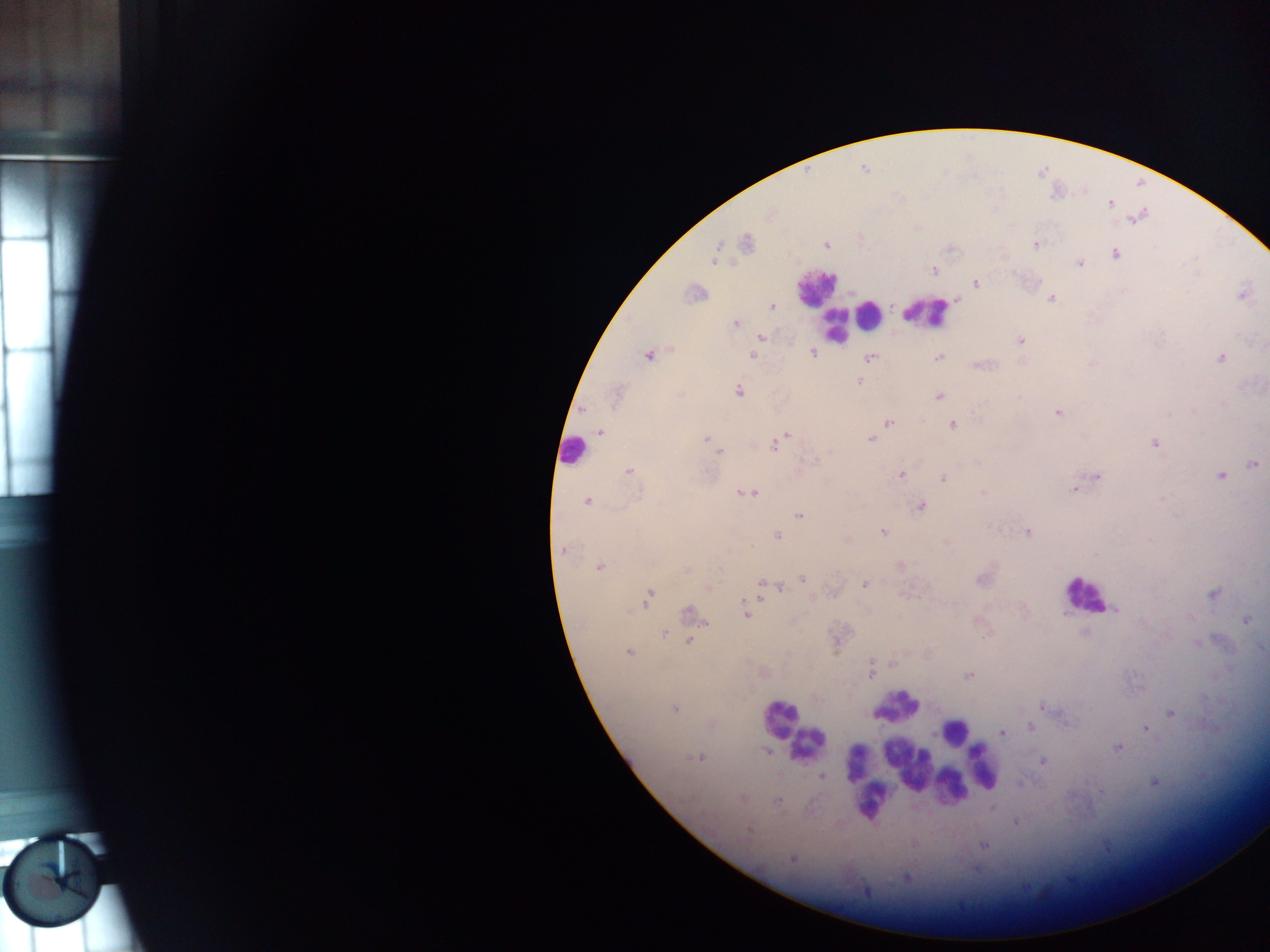
malaria parasite locations = approximate centers as {x, y} in pixels: {863, 167}, {1110, 204}, {746, 242}, {826, 244}, {1035, 244}, {1115, 254}, {716, 255}, {1080, 263}, {933, 269}, {975, 282}, {695, 293}, {1242, 294}, {1050, 298}, {772, 306}, {734, 323}, {760, 337}, {1020, 340}, {813, 352}, {648, 354}, {752, 354}, {938, 357}, {1219, 357}, {870, 358}, {859, 381}, {738, 391}, {616, 395}, {939, 396}, {1058, 412}, {888, 422}, {952, 424}, {599, 432}, {788, 434}, {707, 438}, {869, 439}, {776, 442}, {1154, 442}, {713, 448}, {719, 451}, {1252, 463}, {628, 471}, {901, 474}, {1221, 475}, {1096, 476}, {943, 478}, {1082, 484}, {1075, 488}, {747, 493}, {587, 501}, {920, 506}, {799, 515}, {883, 532}, {1028, 533}, {777, 535}, {563, 550}, {598, 566}, {899, 566}, {686, 569}, {981, 577}, {803, 580}, {864, 584}, {761, 585}, {780, 587}, {708, 588}, {1214, 593}, {647, 598}, {1022, 607}, {1116, 609}, {689, 614}, {747, 614}, {1246, 619}, {1085, 632}, {663, 634}, {691, 637}, {836, 638}, {690, 640}, {1197, 643}, {628, 652}, {870, 670}, {762, 672}, {968, 676}, {1043, 706}, {674, 708}, {1171, 712}, {1030, 727}, {1146, 727}, {1003, 732}, {1118, 747}, {767, 751}, {700, 757}, {1043, 761}, {821, 777}, {1155, 782}, {1019, 784}, {778, 800}, {1015, 821}, {984, 846}, {792, 859}, {907, 878}
leukocyte locations = approximate centers as {x, y} in pixels: {815, 288}, {845, 307}, {926, 313}, {869, 315}, {837, 323}, {572, 451}, {1084, 595}, {896, 707}, {783, 720}, {954, 731}, {807, 743}, {965, 746}, {859, 758}, {911, 766}, {928, 766}, {982, 768}, {970, 771}, {949, 787}, {872, 799}
image size = 1270×952 pixels
preparation = thick blood film
country = Ghana
field of view = single
capture = mobile-phone photograph through a microscope